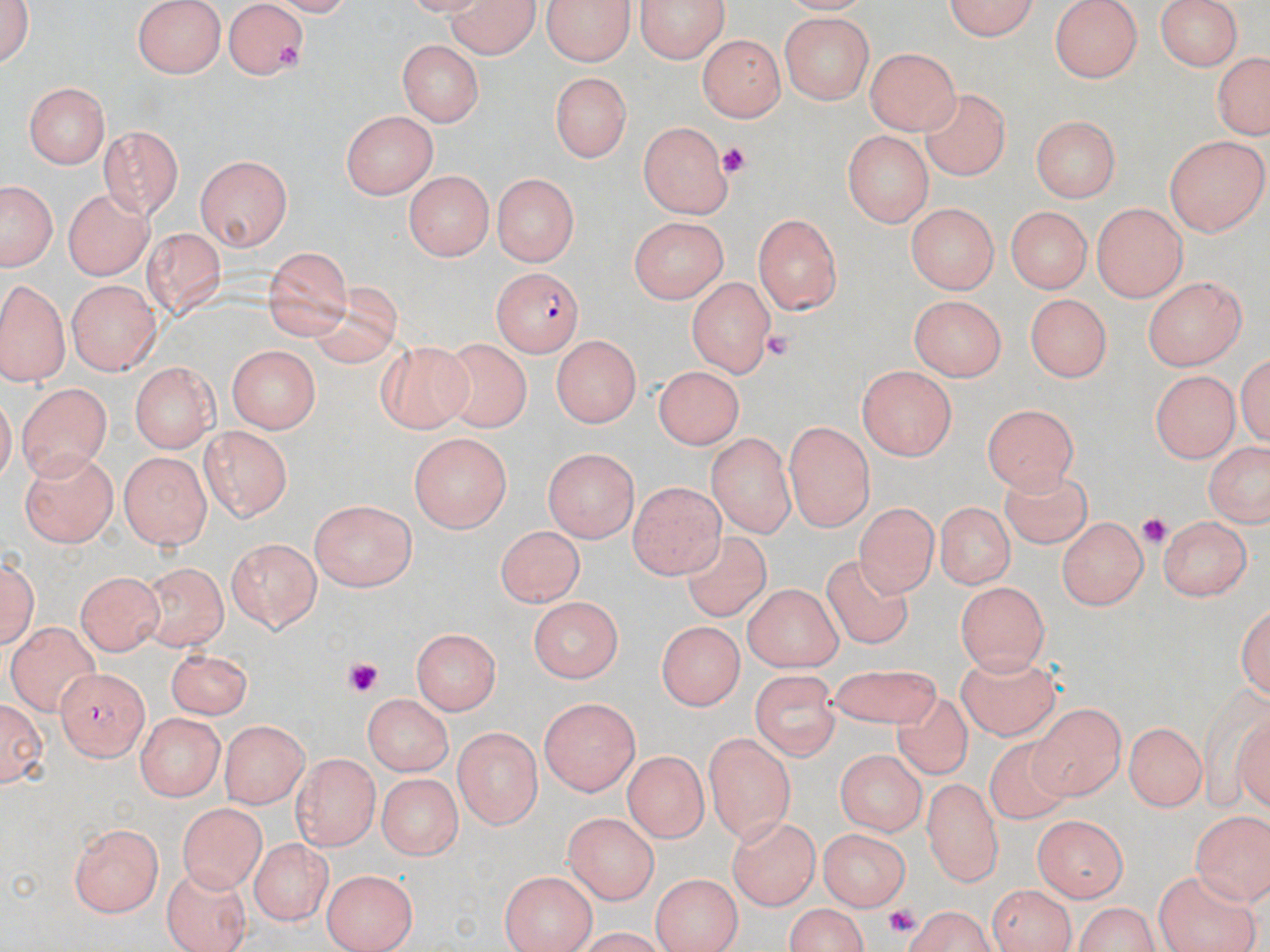

Summary:
  - Coordinate format: approximate bounding boxes as (x1,y1)-(x2,y2) corner pairs in pixels
  - Uninfected red blood cell locations: (1,0)-(38,73), (133,0)-(228,79), (543,0)-(634,64), (637,0)-(726,62), (936,0)-(1042,40), (1050,0)-(1144,81), (1152,0)-(1245,73), (441,1)-(542,56), (223,3)-(313,79), (776,15)-(876,107), (701,33)-(783,122), (396,40)-(484,126), (865,46)-(960,132), (1208,52)-(1270,142), (551,71)-(633,159), (22,79)-(111,170), (922,87)-(1008,181), (341,111)-(435,202), (1030,112)-(1124,201), (637,121)-(737,218), (102,129)-(182,217), (842,129)-(936,224), (1164,135)-(1265,237), (195,153)-(294,251), (404,169)-(493,262), (491,173)-(579,267), (3,186)-(52,270), (65,190)-(154,280), (1091,200)-(1187,301), (905,201)-(1000,295), (1005,205)-(1090,295), (754,213)-(840,315), (631,215)-(729,304), (142,226)-(228,316), (263,244)-(353,339), (0,276)-(69,384), (1141,276)-(1246,369), (686,277)-(775,377), (68,282)-(158,373), (303,284)-(408,370), (1025,292)-(1114,378), (905,294)-(1007,379), (548,334)-(645,425), (378,342)-(473,433), (446,342)-(535,435), (225,343)-(320,433), (133,362)-(219,451), (653,363)-(748,448), (858,365)-(959,458), (1151,368)-(1240,463), (16,380)-(113,478), (984,402)-(1082,493), (783,418)-(876,532), (197,426)-(295,522), (706,432)-(794,538), (409,433)-(514,533), (1200,440)-(1270,528), (542,447)-(641,539), (21,450)-(119,547), (118,451)-(211,551), (995,468)-(1092,559), (628,477)-(723,578), (931,499)-(1015,589), (310,501)-(418,591), (854,504)-(933,596), (1056,515)-(1147,611), (1159,517)-(1251,604), (493,526)-(591,609), (680,531)-(774,619), (223,538)-(323,632), (3,549)-(38,653), (823,552)-(918,652), (141,561)-(228,648), (76,569)-(161,655), (953,579)-(1048,679), (742,580)-(845,672), (526,596)-(625,680), (1236,599)-(1270,704), (653,613)-(748,707), (7,620)-(100,710), (412,628)-(500,715), (166,645)-(253,719), (954,654)-(1064,743), (821,664)-(950,733), (53,667)-(152,758), (749,670)-(843,757), (889,689)-(973,781), (360,694)-(451,777), (539,697)-(641,796), (0,698)-(46,789), (1029,704)-(1124,800), (135,712)-(225,802), (222,720)-(309,807), (1126,723)-(1205,810), (453,727)-(541,828), (981,729)-(1073,830), (702,732)-(794,841), (836,746)-(928,834), (623,749)-(707,842), (294,752)-(379,851), (374,772)-(462,862), (922,774)-(1001,887), (177,801)-(269,891), (1190,808)-(1270,902), (564,812)-(660,906), (729,813)-(819,911), (1033,818)-(1125,901), (69,824)-(166,917), (820,829)-(911,912), (248,837)-(331,925), (1150,863)-(1260,951), (161,867)-(254,946), (323,868)-(417,948), (500,870)-(595,952), (651,872)-(741,952), (985,883)-(1078,952), (906,898)-(993,949), (1068,898)-(1166,952), (781,904)-(874,952)
  - Platelet locations: (716,143)-(752,181), (762,327)-(795,363), (1139,510)-(1172,549), (340,657)-(387,698), (882,901)-(926,932)
  - Plasmodium falciparum-infected red blood cell locations: (490,266)-(586,355)
  - Slide-level diagnosis: Plasmodium falciparum
  - Modality: light microscopy
  - Image size: 1270×952 pixels
  - Magnification: 1000x
  - Preparation: thin blood film
  - Stain: May-Grünwald-Giemsa
  - Field of view: one of a larger specimen